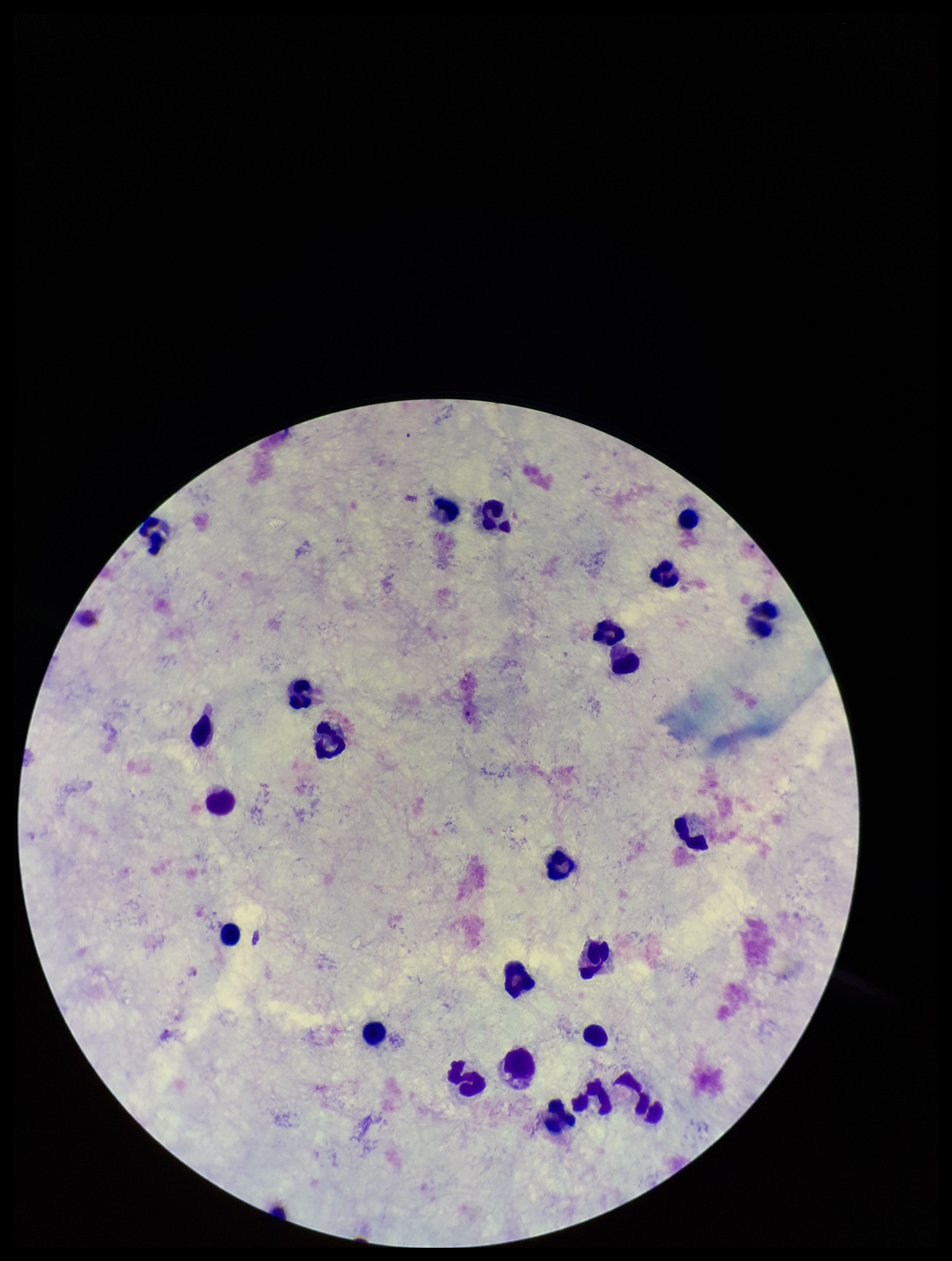
species reported for this patient = Plasmodium vivax
image size = 952×1261 pixels
patient malaria status = positive
capture = smartphone photograph through the microscope eyepiece
parasite count = 0
leukocyte count = 25
preparation = thick smear
field of view = single
Plasmodium parasites = none seen
stain = Giemsa